Identify the parasite.
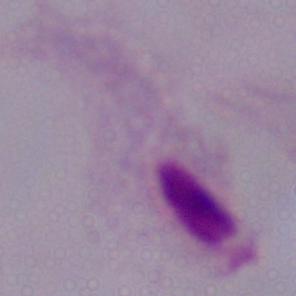
This is a trichomonad.

Summary:
  - Modality: micrograph
  - Magnification: 1000x